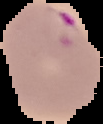
Summary:
  - Image type: segmented cell region on a black background
  - Preparation: thin blood smear
  - Malaria status: parasitized
  - Image size: 103×124 pixels